Assess this cell for malaria.
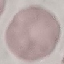
It is uninfected.

Summary:
  - Preparation: thin blood smear
  - Capture: smartphone camera at the microscope eyepiece
  - Stain: Giemsa
  - Image type: automatically extracted cell patch, resized to 64 × 64 pixels